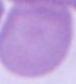

Captured at 1000x magnification. An erythrocyte is seen. Photomicrograph.